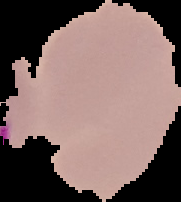
Summary:
  - Image size: 181×202 pixels
  - Preparation: thin blood film
  - Image type: segmented cell region on a black background
  - Result: negative for malaria parasites